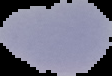 From a thin blood smear. Image is 112×76 pixels. The area outside the segmented cell region is set to black. Result: no Plasmodium parasites detected.